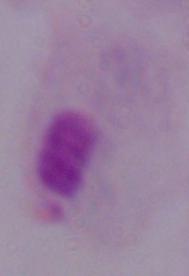

identification = trichomonad
magnification = 1000x
modality = micrograph